Assess this cell for malaria.
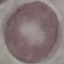

It is uninfected.

Giemsa stain. Thin blood film. Automatically extracted cell patch, resized to 64 × 64 pixels. Photographed with a smartphone camera at the microscope eyepiece.